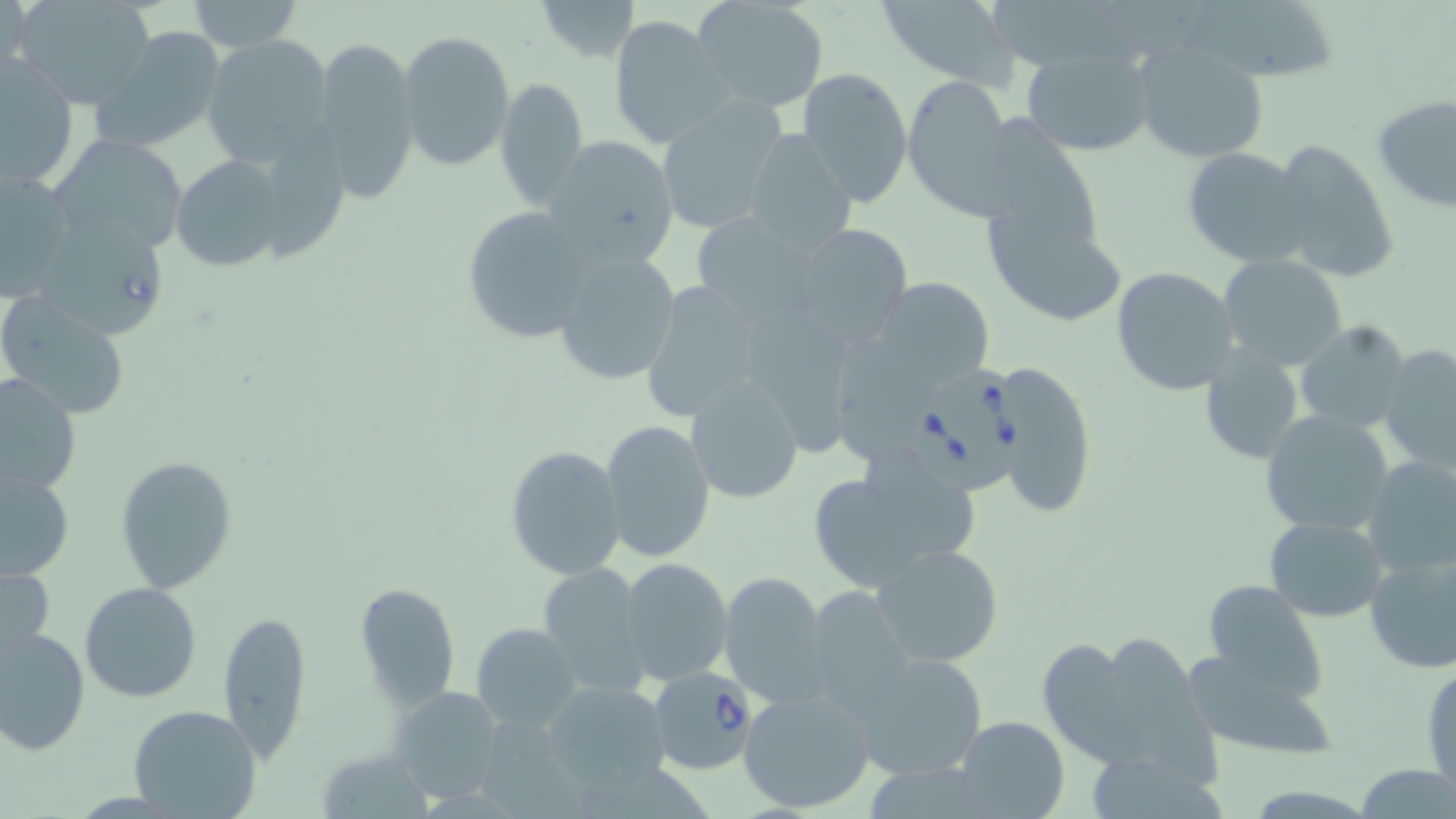

Babesia divergens-infected red blood cell locations = approximate bounding boxes as [x1, y1, x2, y2] in pixels: [908, 374, 1035, 492], [651, 668, 758, 775]
slide-level diagnosis = Babesia divergens
magnification = 1000x
preparation = thin blood smear
field of view = one of a larger specimen
image size = 1456×819 pixels
stain = May-Grünwald-Giemsa
modality = optical microscopy
uninfected red blood cell locations = approximate bounding boxes as [x1, y1, x2, y2] in pixels: [16, 0, 158, 109], [187, 0, 303, 53], [532, 0, 640, 63], [691, 0, 830, 114], [875, 0, 1023, 89], [1184, 1, 1345, 87], [2, 3, 38, 89], [608, 14, 733, 149], [91, 26, 227, 155], [396, 28, 515, 171], [310, 33, 421, 204], [202, 35, 334, 165], [1132, 44, 1270, 164], [1019, 48, 1155, 156], [1, 57, 78, 191], [796, 67, 913, 207], [902, 74, 1018, 219], [495, 75, 590, 213], [1372, 96, 1456, 214], [653, 100, 784, 234], [981, 106, 1115, 249], [742, 129, 858, 259], [48, 134, 190, 260], [543, 135, 679, 266], [1269, 139, 1400, 283], [1183, 147, 1314, 269], [172, 154, 290, 273], [0, 167, 76, 300], [460, 205, 601, 345], [984, 207, 1127, 329], [35, 218, 169, 339], [788, 223, 914, 351], [549, 248, 681, 387], [1219, 254, 1349, 371], [1111, 266, 1240, 395], [869, 276, 998, 392], [638, 279, 767, 422], [0, 296, 129, 419], [744, 311, 871, 458], [1295, 322, 1415, 434], [1279, 337, 1409, 515], [1377, 343, 1456, 476], [1199, 347, 1305, 463], [991, 360, 1097, 520], [2, 371, 81, 499], [685, 379, 805, 506], [1261, 411, 1396, 537], [601, 419, 716, 562], [505, 445, 629, 582], [115, 456, 236, 593], [1359, 456, 1456, 579], [802, 458, 980, 596], [1, 469, 74, 580], [1264, 516, 1388, 622], [871, 543, 1004, 668], [1362, 547, 1456, 675], [619, 558, 735, 687], [537, 561, 650, 694], [0, 562, 55, 664], [718, 572, 832, 707], [1199, 579, 1327, 702], [80, 582, 202, 702], [356, 582, 461, 709], [806, 584, 918, 720], [216, 609, 313, 764], [472, 622, 583, 731], [1, 626, 90, 757], [1044, 630, 1218, 779], [1179, 647, 1340, 759], [854, 653, 986, 782], [1423, 661, 1455, 799], [543, 679, 672, 798], [738, 685, 878, 814], [390, 686, 505, 802], [128, 702, 261, 818], [954, 714, 1069, 819], [318, 747, 432, 819]